Assess this cell for malaria.
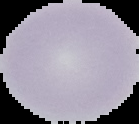

It is uninfected.

image_size: 139×124 pixels
image_type: segmented cell region on a black background
preparation: thin blood smear